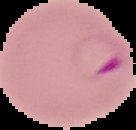
Summary:
  - Image size: 136×130 pixels
  - Image type: cell region segmented out of the field of view; surrounding area masked to black
  - Preparation: thin blood smear
  - Result: Plasmodium parasites identified